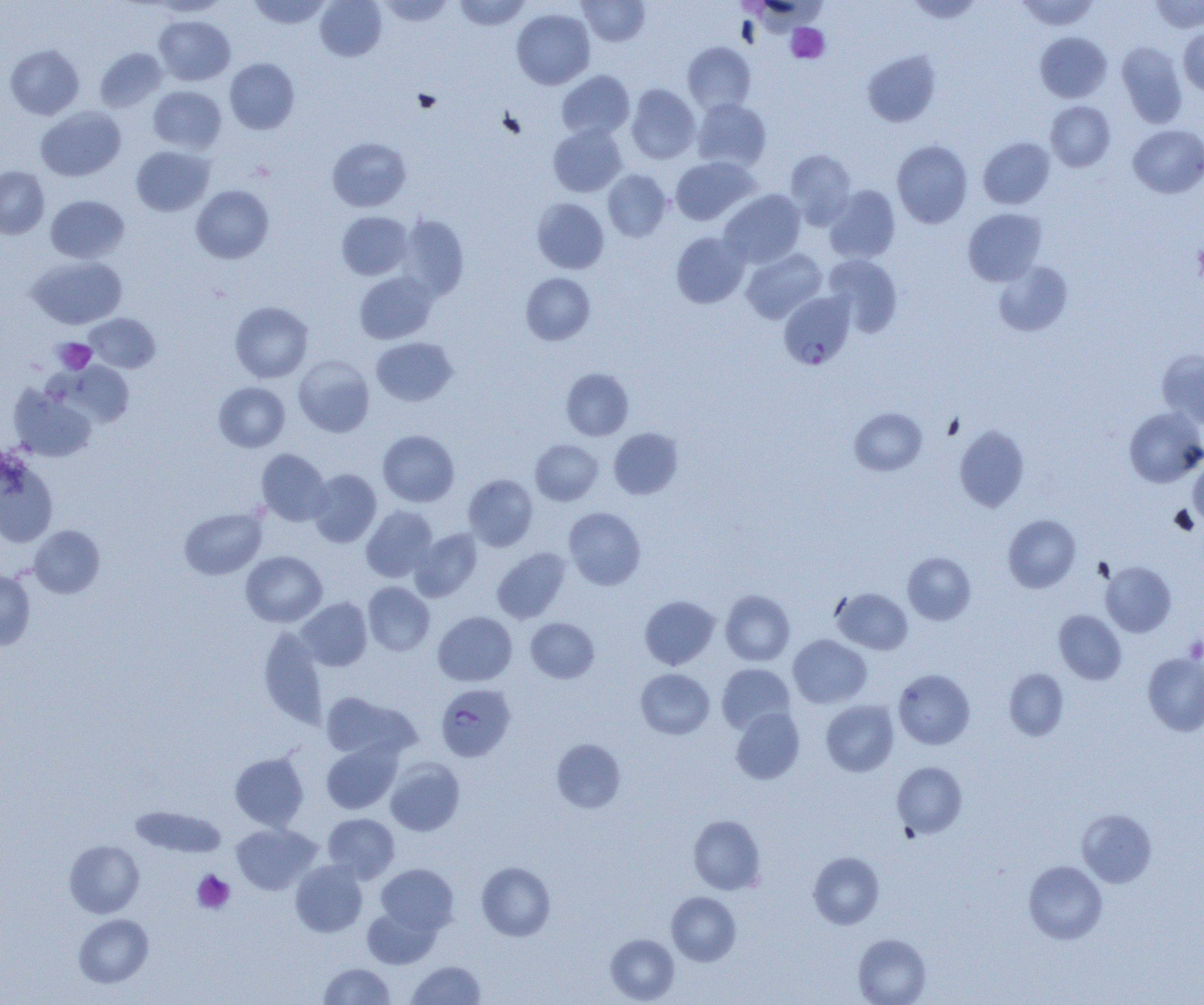 Approximate bounding boxes as (x1,y1)-(x2,y2) corner pairs in pixels. Plasmodium falciparum-infected red blood cell locations: (779,292)-(856,369), (438,686)-(519,764). Platelet locations: (786,23)-(829,62), (1193,242)-(1204,283), (54,338)-(96,374), (1184,637)-(1204,663), (192,870)-(235,914). Uninfected red blood cell locations: (247,0)-(331,29), (315,0)-(386,61), (377,0)-(453,26), (454,0)-(531,30), (577,0)-(650,46), (1016,0)-(1099,31), (1152,0)-(1203,32), (149,1)-(229,17), (906,1)-(983,23), (511,8)-(595,89), (154,15)-(235,85), (1178,27)-(1204,95), (1035,32)-(1111,103), (682,42)-(756,114), (1116,42)-(1187,127), (5,45)-(84,119), (95,48)-(167,112), (862,51)-(940,127), (225,58)-(299,134), (556,70)-(635,141), (627,84)-(700,164), (148,85)-(227,154), (691,98)-(771,172), (1046,101)-(1115,172), (36,106)-(125,181), (548,124)-(627,197), (1128,124)-(1204,198), (327,137)-(411,212), (978,137)-(1055,209), (892,140)-(972,228), (131,146)-(214,216), (785,149)-(856,227), (670,156)-(759,225), (0,167)-(49,239), (603,169)-(671,241), (191,185)-(274,264), (824,185)-(901,263), (720,189)-(806,267), (46,195)-(128,263), (532,198)-(609,274), (963,208)-(1047,286), (337,211)-(413,280), (397,214)-(469,302), (671,232)-(749,308), (741,248)-(827,323), (823,254)-(903,336), (27,256)-(127,329), (993,260)-(1073,336), (354,272)-(437,344), (520,273)-(595,345), (230,301)-(314,383), (86,313)-(160,373), (371,337)-(457,406), (1157,349)-(1204,427), (293,355)-(374,437), (66,362)-(134,426), (561,368)-(634,440), (214,382)-(290,452), (9,385)-(97,462), (850,407)-(927,475), (1124,407)-(1204,487), (954,424)-(1029,512), (609,428)-(683,499), (378,430)-(459,507), (530,439)-(603,505), (256,449)-(331,525), (0,456)-(58,548), (1189,460)-(1204,527), (308,469)-(381,547), (463,474)-(538,551), (361,505)-(437,582), (563,507)-(646,590), (179,508)-(266,579), (1003,514)-(1080,592), (29,525)-(104,598), (410,529)-(482,601), (492,547)-(570,623), (240,551)-(327,627), (903,552)-(976,624), (1101,561)-(1176,637), (0,569)-(35,650), (362,582)-(435,656), (832,588)-(912,654), (720,590)-(795,665), (639,595)-(720,669), (297,597)-(372,671), (1054,610)-(1126,684), (433,611)-(517,686), (526,617)-(599,683), (259,627)-(329,728), (787,634)-(872,708), (1143,652)-(1204,736), (717,663)-(795,735), (635,668)-(714,739), (1003,668)-(1068,740), (893,669)-(975,749), (321,692)-(417,761), (821,700)-(899,776), (731,708)-(805,784), (551,739)-(626,813), (321,741)-(401,814), (230,752)-(308,830), (385,758)-(465,836), (892,761)-(967,838), (129,805)-(227,858), (1077,809)-(1157,888), (323,813)-(399,882), (688,815)-(766,895), (230,823)-(321,895), (64,840)-(144,918), (808,852)-(884,929), (290,860)-(367,937), (1023,860)-(1107,944), (477,861)-(556,941), (376,863)-(458,935), (666,892)-(741,966), (362,906)-(440,969), (74,913)-(154,987), (605,934)-(680,1003), (853,934)-(931,1005), (408,960)-(486,1005), (319,963)-(395,1005). Slide-level diagnosis: Plasmodium falciparum. Thin blood smear. Image is 1204×1005 pixels. Captured at 1000x magnification. One field of a larger specimen. Light microscopy.